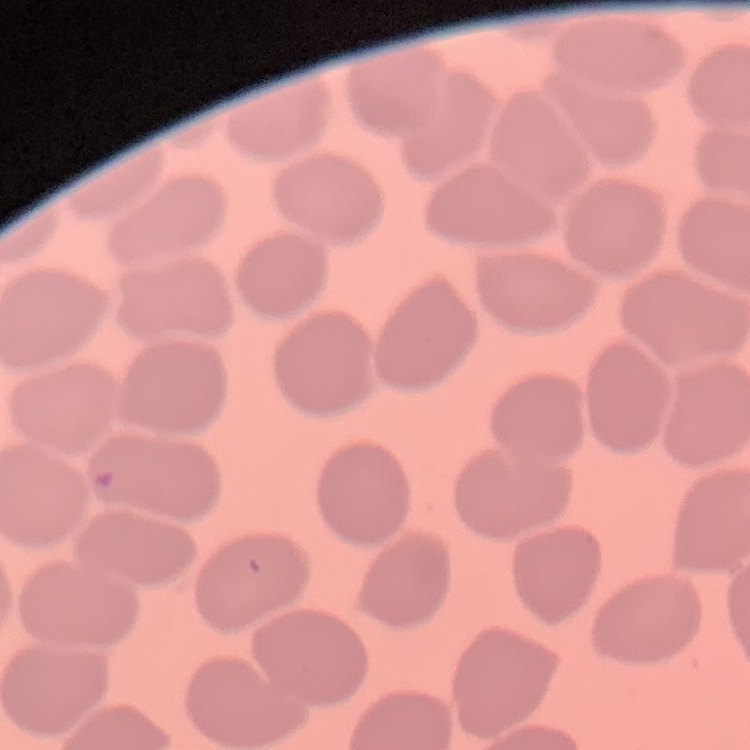
{
  "erythrocyte_morphology": "no rouleaux formation",
  "stain": "Field's or Giemsa",
  "preparation": "thin peripheral smear",
  "image_type": "square crop of a larger photomicrograph"
}